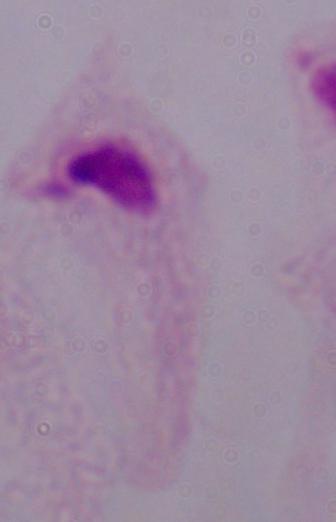
Summary:
  - Modality: photomicrograph
  - Identification: trichomonad
  - Magnification: 1000x